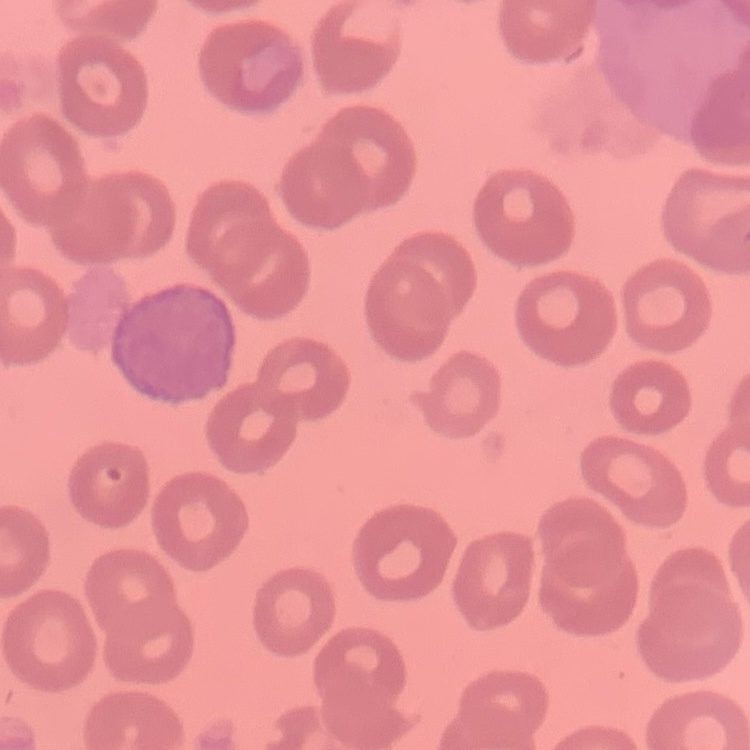

red blood cell morphology = no rouleaux formation
image type = one tile cut from a larger photomicrograph
preparation = thin blood film
stain = Field's or Giemsa